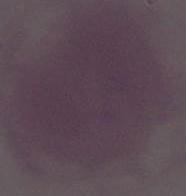
Summary:
  - Magnification: 1000x
  - Identification: red blood cell
  - Modality: micrograph